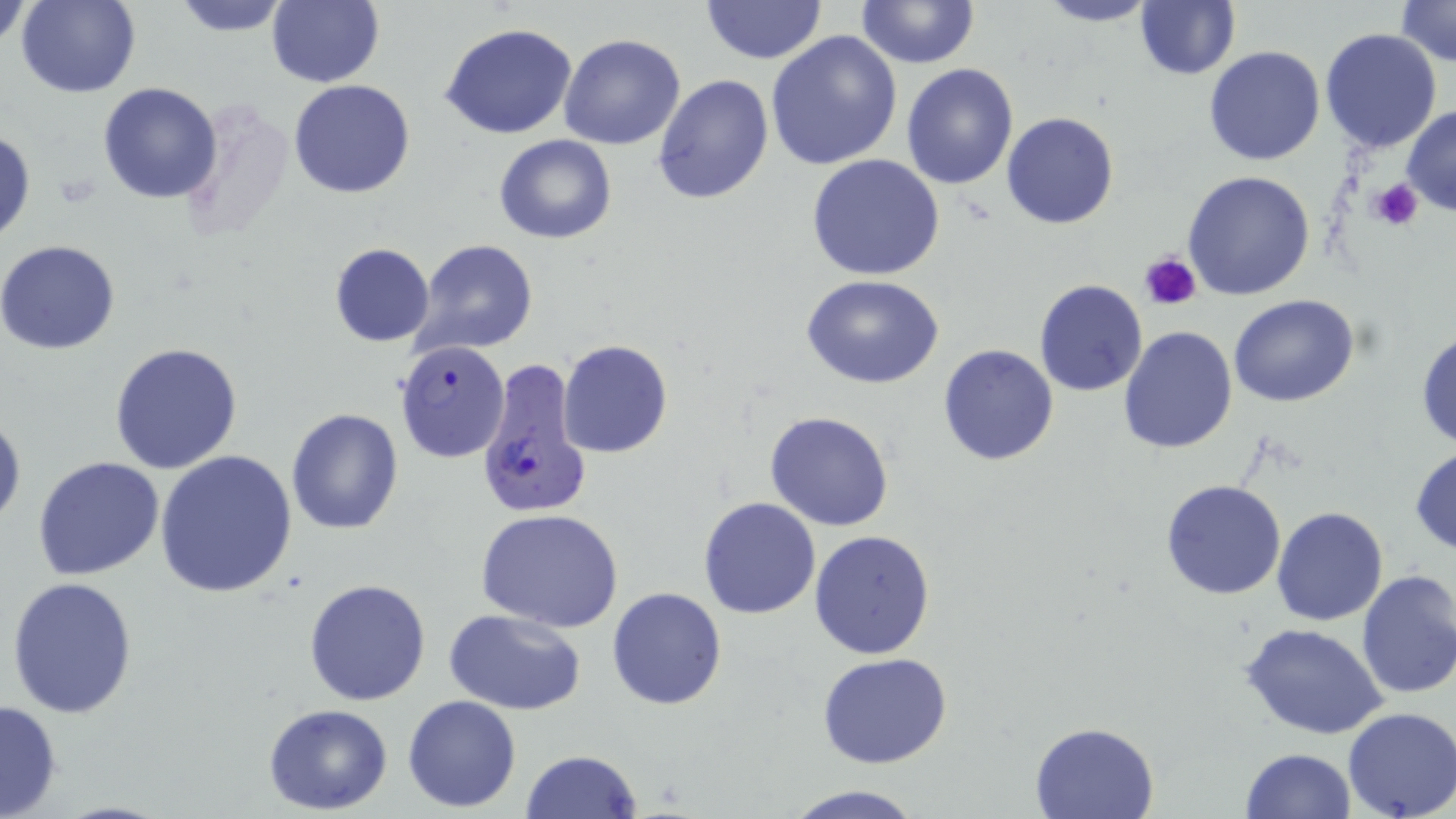
slide_level_diagnosis: Plasmodium falciparum
platelet_locations: 'approximate bounding boxes as (x1, y1, x2, y2) in pixels: (1368, 178, 1425, 231), (1140, 250, 1203, 311)'
magnification: 1000x
preparation: thin blood film
uninfected_red_blood_cell_locations: 'approximate bounding boxes as (x1, y1, x2, y2) in pixels: (1, 0, 33, 51), (15, 0, 142, 97), (167, 0, 297, 36), (265, 0, 385, 88), (699, 0, 827, 64), (854, 0, 981, 69), (1032, 0, 1162, 27), (1393, 1, 1455, 69), (1134, 2, 1240, 80), (440, 21, 580, 139), (1319, 29, 1442, 153), (765, 30, 904, 171), (559, 33, 686, 150), (1204, 45, 1327, 166), (900, 62, 1019, 190), (653, 75, 775, 206), (288, 80, 416, 199), (97, 82, 221, 204), (1402, 106, 1456, 218), (1001, 112, 1119, 229), (1, 125, 36, 246), (494, 135, 617, 243), (806, 154, 947, 281), (1182, 170, 1316, 301), (413, 239, 539, 354), (0, 241, 121, 355), (328, 243, 436, 347), (801, 275, 948, 390), (1034, 280, 1149, 396), (1229, 293, 1359, 407), (1117, 325, 1238, 452), (1415, 328, 1456, 450), (557, 340, 672, 458), (109, 341, 243, 474), (937, 345, 1059, 465), (286, 408, 405, 535), (764, 409, 895, 531), (0, 410, 25, 532), (1409, 445, 1456, 556), (155, 451, 300, 598), (32, 456, 165, 581), (1159, 479, 1287, 600), (698, 497, 822, 620), (1270, 506, 1390, 626), (475, 508, 624, 631), (808, 529, 937, 661), (1354, 568, 1456, 701), (5, 575, 139, 720), (304, 578, 431, 706), (607, 587, 728, 710), (444, 608, 589, 713), (1240, 621, 1389, 740), (818, 653, 953, 769), (403, 694, 522, 811), (1, 698, 64, 819), (263, 703, 395, 815), (1341, 708, 1455, 819), (1029, 721, 1161, 819), (1239, 747, 1357, 819), (520, 750, 643, 819), (780, 783, 928, 819)'
image_size: 1456×819 pixels
field_of_view: one of a larger specimen
stain: May-Grünwald-Giemsa
plasmodium_falciparum_infected_red_blood_cell_locations: 'approximate bounding boxes as (x1, y1, x2, y2) in pixels: (395, 341, 509, 463), (477, 362, 592, 519)'
modality: light microscopy